Describe the morphology of the red blood cells.
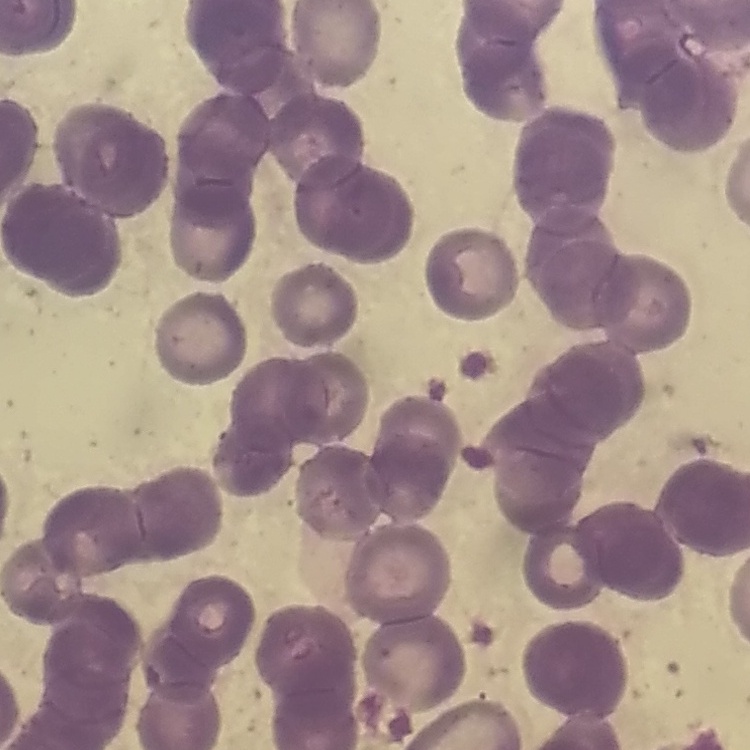
Rouleaux formation.

image type = square crop of a larger photomicrograph
preparation = thin blood film
stain = Field's or Giemsa